State the blood parasite species.
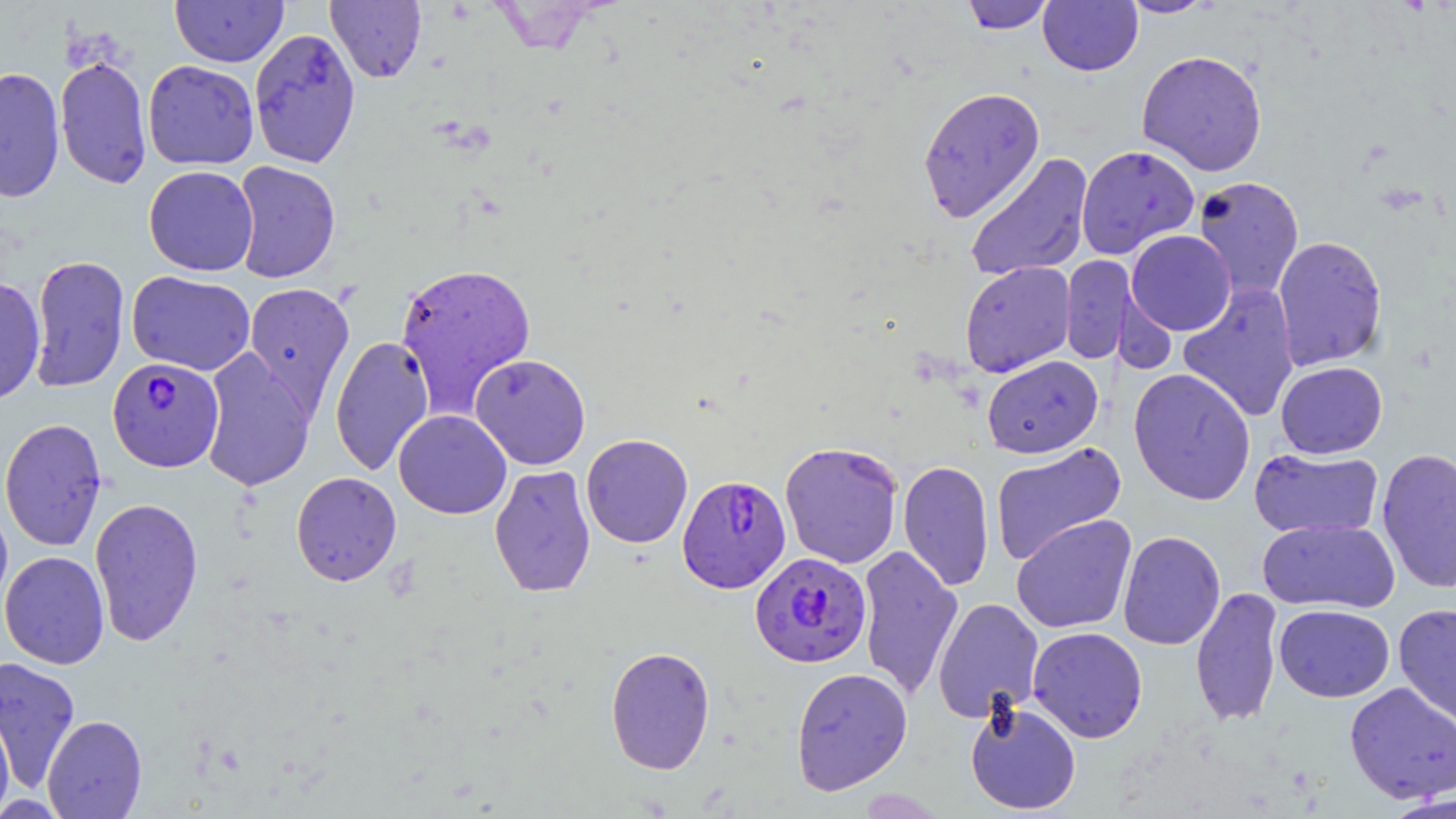
Plasmodium falciparum.

Summary:
  - Coordinate format: approximate bounding boxes as (x1, y1, x2, y2) in pixels
  - Plasmodium falciparum-infected red blood cell locations: (107, 357, 224, 472), (677, 475, 791, 593), (750, 551, 871, 669)
  - Uninfected red blood cell locations: (170, 0, 288, 67), (326, 0, 427, 83), (959, 0, 1055, 34), (1118, 0, 1219, 18), (1038, 1, 1143, 75), (249, 28, 361, 169), (1136, 49, 1268, 176), (54, 55, 152, 189), (142, 60, 259, 170), (0, 67, 66, 202), (917, 85, 1045, 223), (1075, 144, 1200, 259), (964, 152, 1093, 282), (231, 161, 341, 284), (143, 165, 259, 276), (1192, 176, 1305, 302), (1126, 230, 1236, 336), (1272, 235, 1388, 371), (29, 254, 130, 393), (1060, 254, 1134, 365), (959, 261, 1076, 377), (395, 262, 536, 416), (127, 270, 256, 375), (0, 278, 46, 406), (243, 281, 355, 416), (1177, 282, 1300, 423), (329, 335, 435, 477), (199, 349, 315, 493), (470, 353, 591, 470), (981, 355, 1103, 458), (1275, 361, 1388, 459), (1128, 368, 1256, 505), (393, 410, 512, 519), (0, 417, 107, 552), (580, 433, 693, 548), (779, 440, 904, 569), (990, 442, 1127, 566), (1249, 447, 1383, 540), (1376, 447, 1456, 595), (898, 460, 995, 592), (489, 464, 596, 598), (291, 471, 402, 586), (89, 496, 204, 647), (0, 499, 13, 619), (1011, 514, 1137, 634), (1257, 518, 1399, 613), (1117, 531, 1226, 650), (856, 545, 963, 701), (0, 551, 110, 669), (1190, 587, 1283, 728), (932, 597, 1044, 723), (1394, 603, 1456, 729), (1274, 604, 1394, 702), (1027, 626, 1147, 743), (605, 646, 716, 774), (0, 656, 81, 792), (790, 666, 913, 795), (1343, 682, 1456, 804), (964, 699, 1081, 815), (0, 708, 15, 815), (42, 715, 147, 818), (856, 787, 948, 818), (1383, 794, 1456, 818)
  - Field of view: one of a larger specimen
  - Magnification: 1000x
  - Image size: 1456×819 pixels
  - Preparation: thin blood smear
  - Modality: light microscopy
  - Stain: May-Grünwald-Giemsa